Locate and identify every blood parasite.
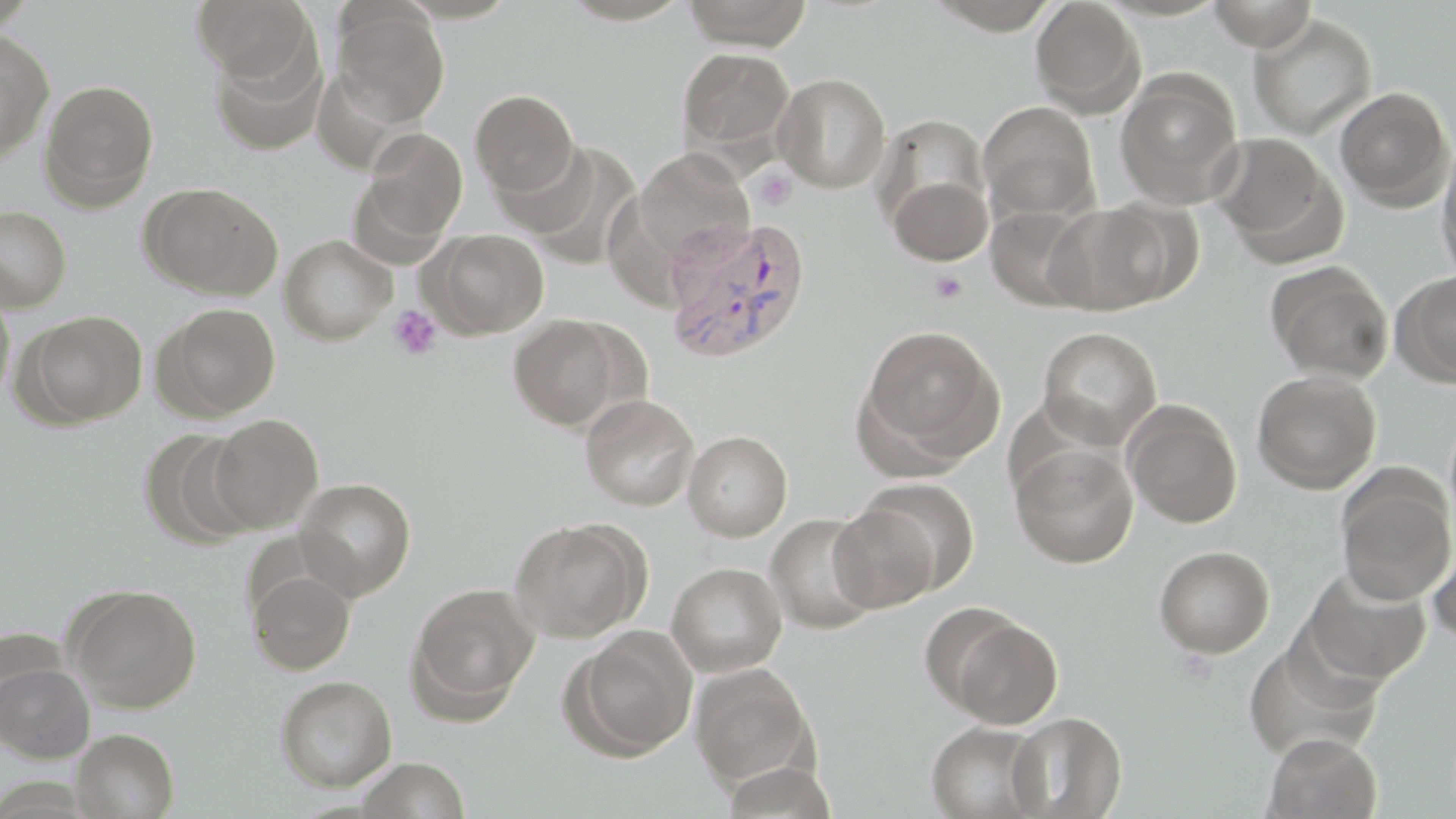
Approximate bounding boxes as (x1,y1)-(x2,y2) corner pairs in pixels.
Plasmodium vivax-infected red blood cells: (662,215)-(812,363).
No Plasmodium falciparum, Plasmodium ovale, Plasmodium malariae, Babesia divergens, or Trypanosoma brucei observed.

Uninfected red blood cell locations: (191,0)-(314,82), (680,0)-(814,50), (1030,0)-(1145,116), (1208,0)-(1318,52), (923,1)-(1066,33), (332,4)-(450,126), (1248,14)-(1377,139), (0,30)-(55,161), (210,38)-(327,156), (677,48)-(795,157), (773,72)-(891,192), (1115,73)-(1243,208), (39,81)-(158,210), (1335,86)-(1454,210), (470,89)-(579,197), (978,101)-(1100,221), (872,114)-(991,237), (358,127)-(467,246), (1209,131)-(1343,261), (1437,140)-(1456,284), (493,141)-(602,238), (520,143)-(641,265), (636,145)-(754,260), (885,172)-(993,266), (142,182)-(282,299), (1043,201)-(1185,315), (0,205)-(72,312), (986,205)-(1096,312), (427,228)-(549,339), (279,235)-(396,345), (1264,262)-(1395,384), (1391,270)-(1456,388), (0,290)-(15,406), (156,303)-(281,420), (20,310)-(149,428), (508,313)-(633,431), (857,324)-(1002,466), (1037,326)-(1162,449), (1251,369)-(1382,494), (580,393)-(700,511), (1123,402)-(1242,529), (207,414)-(323,532), (141,428)-(258,548), (683,430)-(792,541), (1010,442)-(1138,568), (1336,473)-(1455,604), (295,478)-(416,599), (855,478)-(979,595), (827,504)-(940,612), (765,512)-(881,634), (509,518)-(649,643), (1428,537)-(1456,647), (1153,545)-(1275,658), (666,562)-(787,677), (1299,565)-(1433,687), (246,566)-(355,675), (408,582)-(540,715), (65,583)-(203,713), (943,612)-(1064,729), (569,626)-(698,759), (0,661)-(94,763), (690,662)-(817,789), (273,675)-(397,791), (1005,712)-(1126,818), (925,722)-(1048,819), (71,728)-(179,819), (1261,732)-(1383,818), (354,757)-(471,818). Platelet locations: (755,168)-(797,210), (929,269)-(969,305), (388,305)-(443,362). Slide-level diagnosis: Plasmodium vivax. Thin blood smear. Image is 1456×819 pixels. May-Grünwald-Giemsa stain. Captured at 1000x magnification. One field of a larger specimen. Light microscopy.